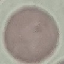

Malaria status: uninfected. Photographed with a smartphone camera at the microscope eyepiece. Thin blood film. Giemsa-stained preparation. Automatically extracted cell patch, resized to 64 × 64 pixels.